Outline every malaria parasite.
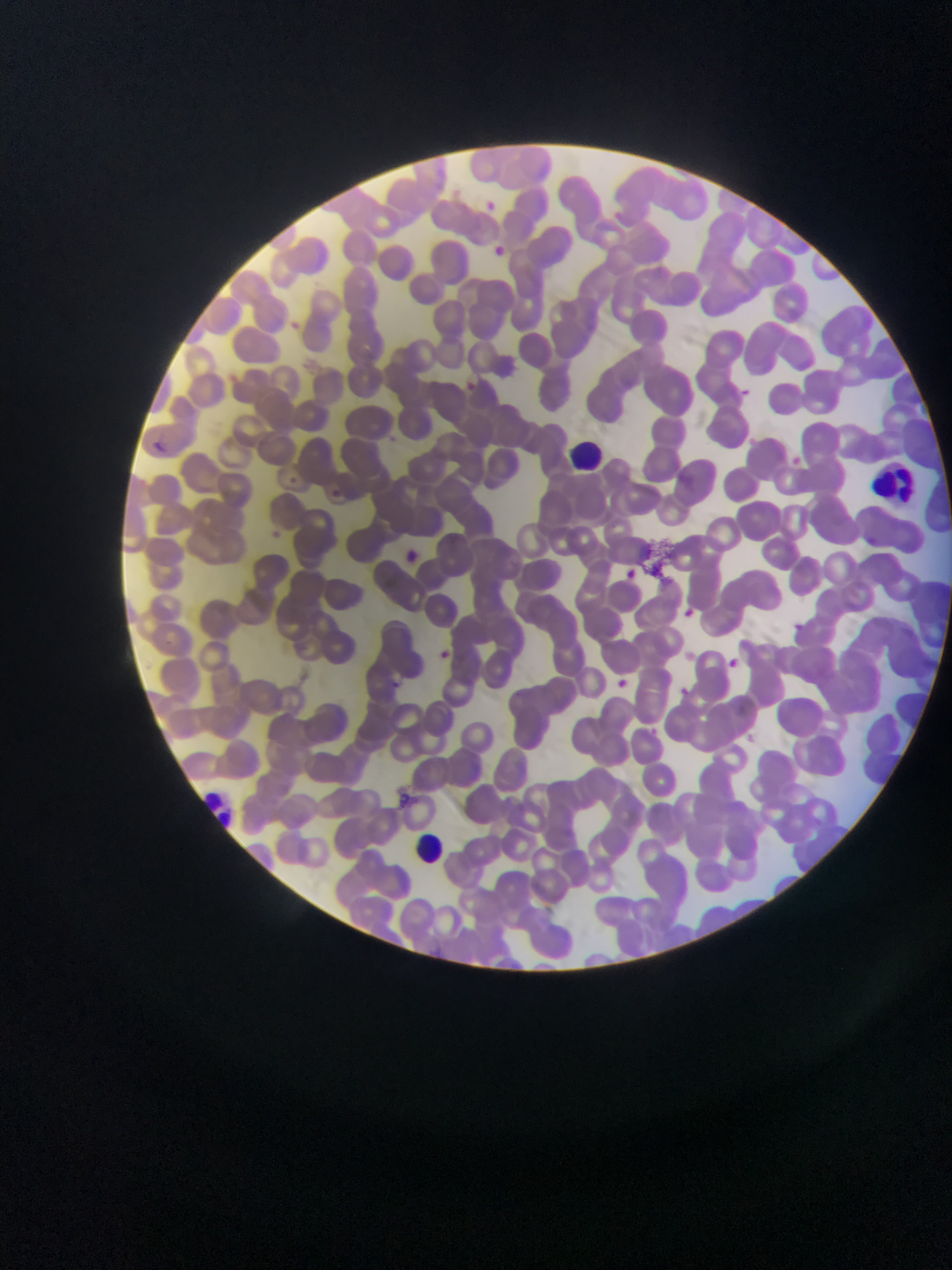

No malaria parasites observed.

image size = 952×1270 pixels
preparation = thin blood film
field of view = single
country = Ghana
capture = mobile-phone photograph through a microscope
leukocyte locations = approximate bounding boxes as {left, top, right, bottom} in pixels: {565, 430, 608, 486}, {874, 458, 928, 515}, {193, 783, 236, 824}, {400, 825, 451, 876}